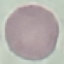

Summary:
  - Result: negative for malaria parasites
  - Image type: cell patch, automatically extracted from a larger field of view and resized to 64 × 64 pixels
  - Stain: Giemsa
  - Preparation: thin blood film
  - Capture: smartphone camera at the microscope eyepiece